Assess this cell for malaria.
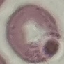
Uninfected.

Summary:
  - Stain: Giemsa
  - Capture: smartphone camera at the microscope eyepiece
  - Image type: cell patch, automatically extracted from a larger field of view and resized to 64 × 64 pixels
  - Preparation: thin blood smear